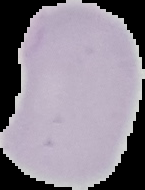
image size = 145×190 pixels
preparation = thin blood smear
result = negative for malaria parasites
image type = cell region segmented out of the field of view; surrounding area masked to black